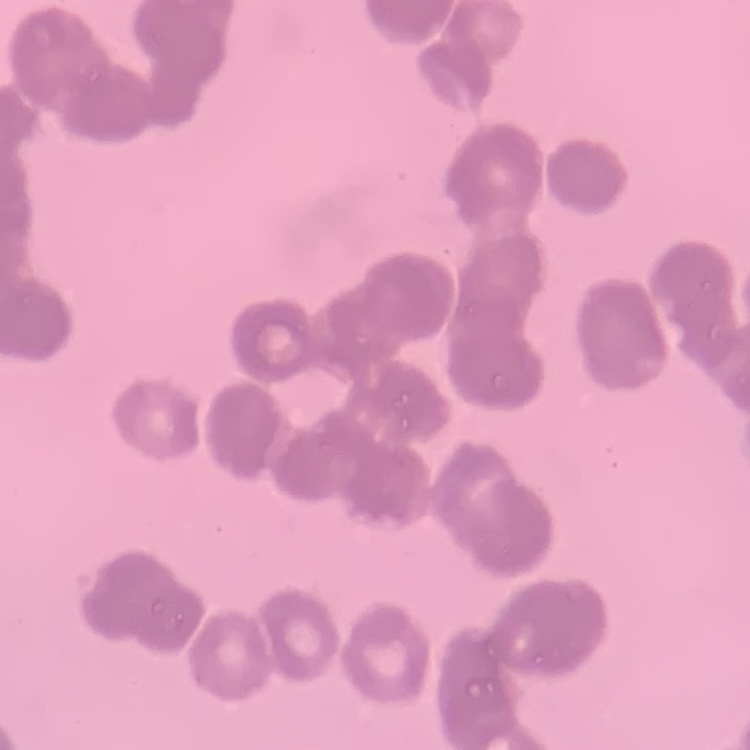
The red blood cells exhibit rouleaux formation. Thin peripheral smear. One tile cut from a larger photomicrograph. Stained with either Field's or Giemsa.